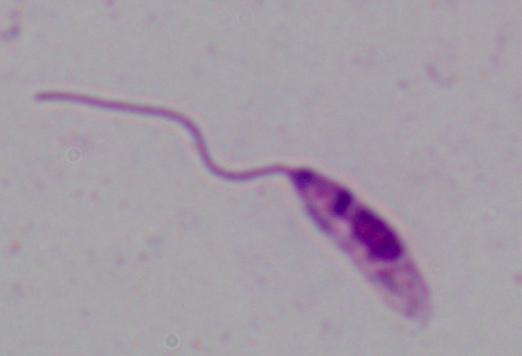

identification = Leishmania
magnification = 1000x
modality = micrograph